State which parasite is depicted.
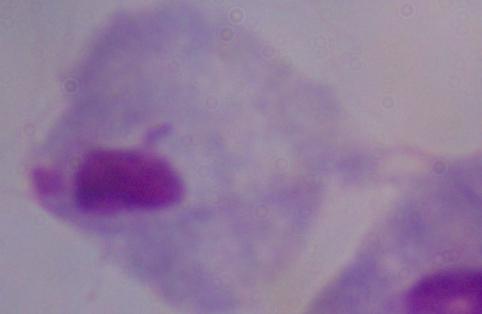

This is a trichomonad.

{
  "magnification": "1000x",
  "modality": "photomicrograph"
}